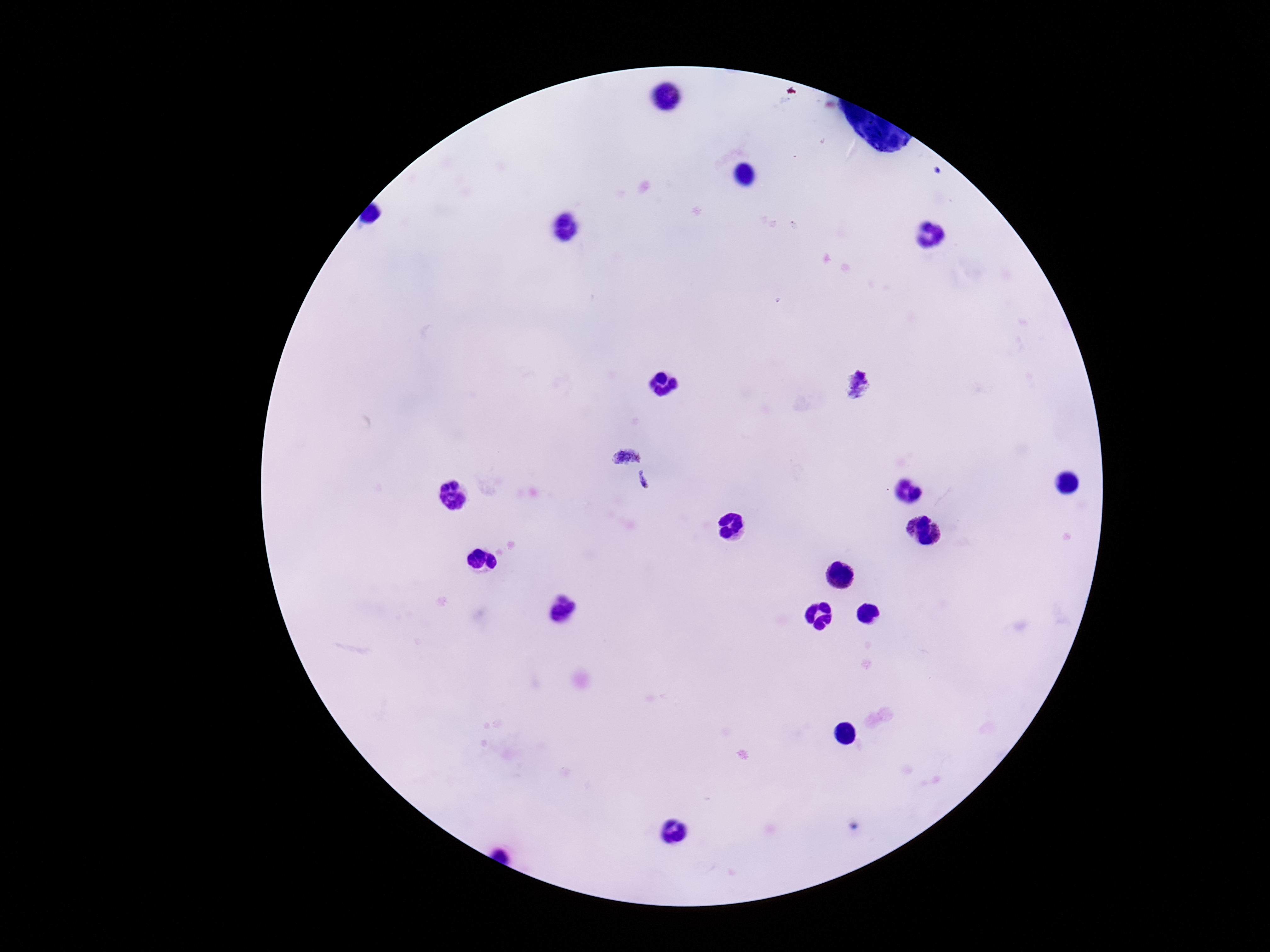

Approximate object centers, in pixels from the top-left corner. Plasmodium parasite locations: (x=857, y=385), (x=627, y=451), (x=643, y=483). 100x magnification. Photographed through the microscope eyepiece with a smartphone camera. Image is 1270×952 pixels. Giemsa stain. Patient malaria status: infected. Thick peripheral-blood smear. One field from this slide.